Classify this cell by malaria status.
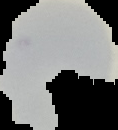
It is uninfected.

From a thin blood film. Segmented cell region on a black background. Image is 118×130 pixels.